Assess this cell for malaria.
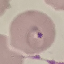
It is parasitized.

stain = Giemsa
capture = smartphone camera at the microscope eyepiece
image type = cell patch, automatically extracted from a larger field of view and resized to 64 × 64 pixels
preparation = thin blood smear